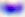
Toxoplasma gondii is shown. Micrograph. Captured at 400x magnification.